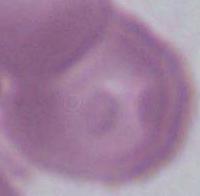
Captured at 1000x magnification. Micrograph. An erythrocyte is seen.